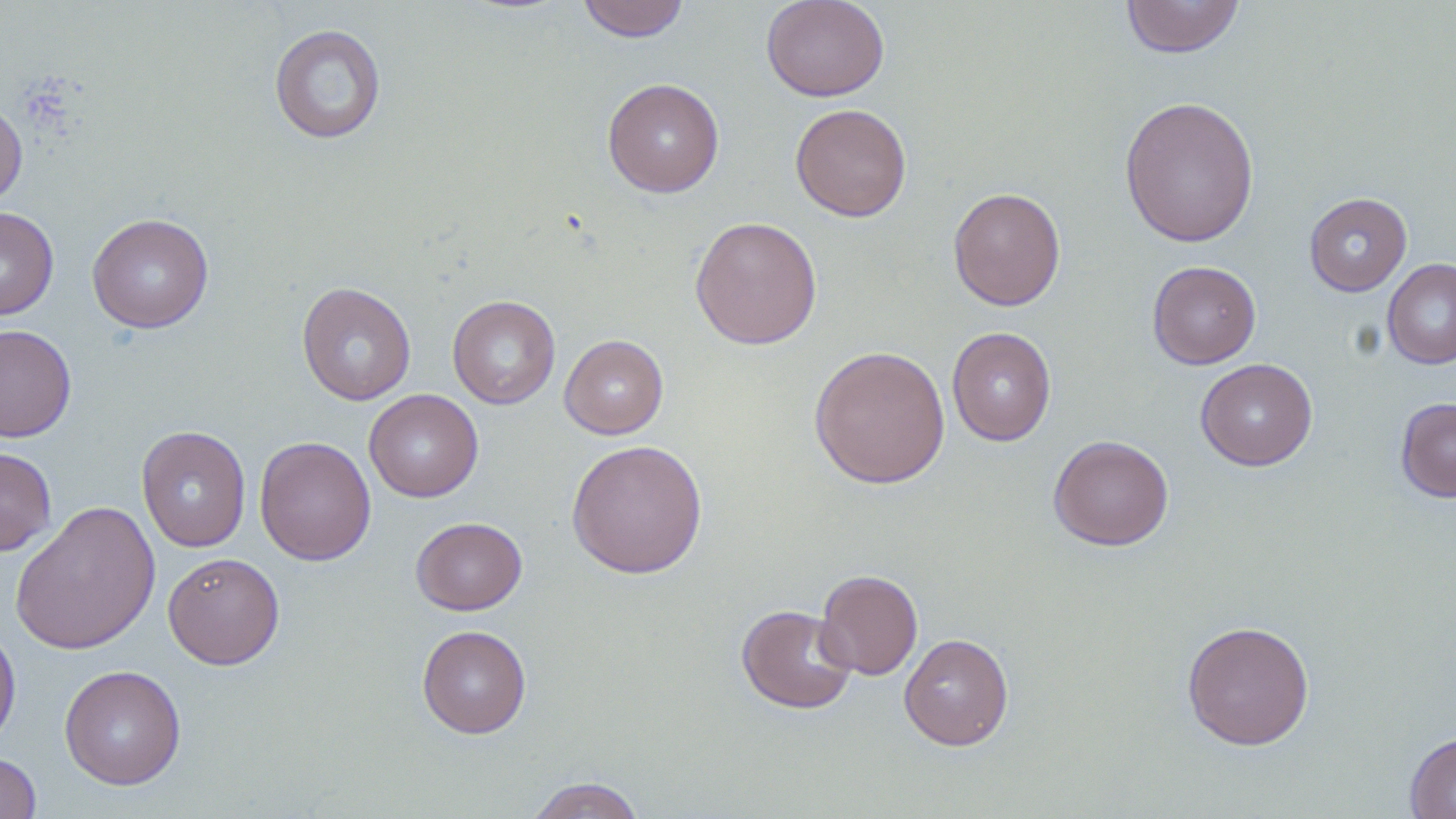

Approximate bounding boxes as [x1, y1, x2, y2] in pixels. Uninfected red blood cell locations: [576, 0, 690, 42], [761, 0, 890, 102], [1120, 0, 1244, 58], [269, 23, 387, 144], [602, 78, 725, 198], [1119, 95, 1260, 248], [0, 97, 27, 208], [790, 103, 912, 222], [948, 186, 1066, 311], [1304, 192, 1412, 296], [0, 207, 58, 321], [87, 213, 214, 333], [689, 216, 822, 350], [1382, 258, 1456, 370], [1147, 260, 1261, 369], [296, 282, 416, 406], [448, 296, 560, 409], [0, 323, 77, 443], [946, 327, 1056, 446], [559, 334, 668, 439], [809, 345, 950, 489], [1196, 358, 1317, 471], [363, 389, 483, 502], [1395, 397, 1456, 502], [136, 425, 251, 552], [1048, 434, 1174, 551], [254, 436, 376, 566], [566, 439, 708, 579], [0, 446, 57, 556], [10, 500, 161, 656], [410, 517, 527, 615], [162, 552, 285, 669], [815, 569, 923, 680], [736, 604, 858, 715], [1181, 619, 1314, 750], [0, 623, 21, 749], [417, 624, 532, 739], [899, 633, 1014, 751], [59, 665, 186, 790], [1404, 730, 1456, 819], [0, 753, 41, 818], [524, 776, 647, 819]. Slide-level diagnosis: no evidence of blood parasites. May-Grünwald-Giemsa stain. Light microscopy. Single field of view. Captured at 1000x magnification. Thin blood smear. Image is 1456×819 pixels.